State which parasite is depicted.
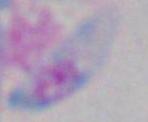
Toxoplasma gondii.

{
  "modality": "photomicrograph",
  "magnification": "1000x"
}